Report the malaria status of this cell.
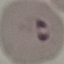

Parasitized.

stain: Giemsa
preparation: thin blood smear
image_type: automatically extracted cell patch, resized to 64 × 64 pixels
capture: smartphone camera at the microscope eyepiece